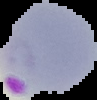
image type = segmented cell region on a black background
image size = 97×100 pixels
preparation = thin blood film
result = malaria parasites identified